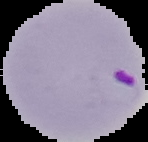

result = malaria parasites identified
image size = 148×142 pixels
preparation = thin blood film
image type = segmented cell region with the area outside set to black